Comment on the morphology of the red blood cells.
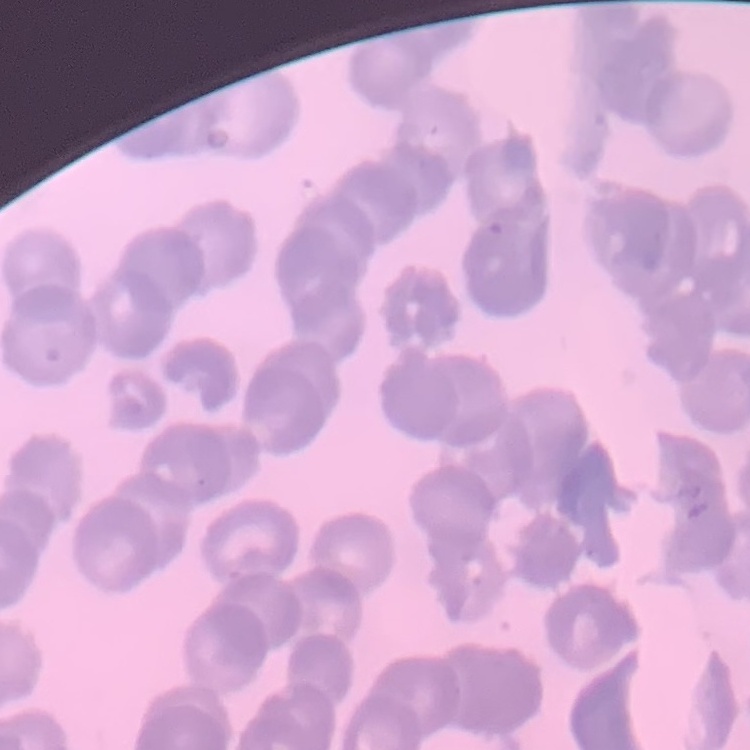

Rouleaux formation.

stain: Field's or Giemsa
preparation: thin peripheral smear
image_type: one tile cut from a larger photomicrograph